Point out each Plasmodium parasite.
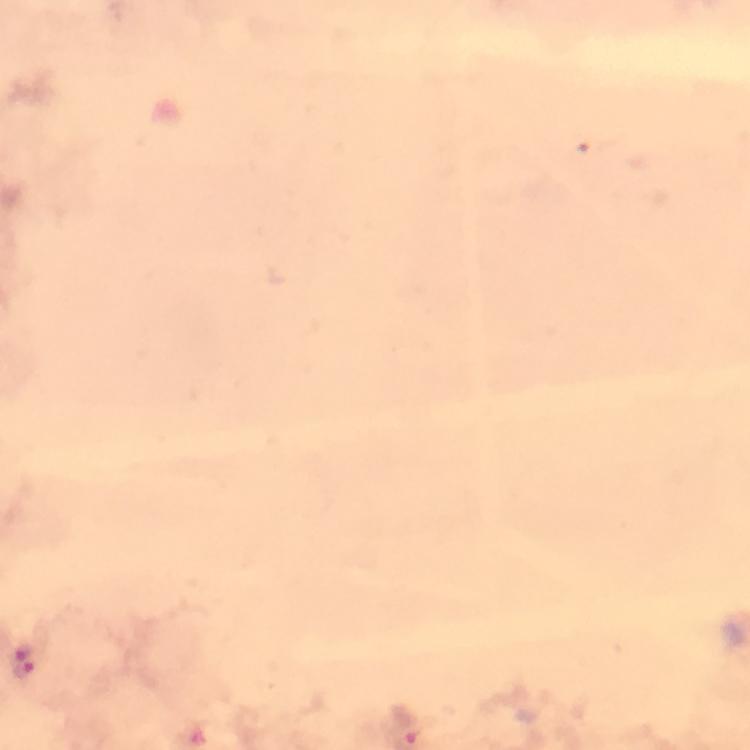

Approximate centers as {x, y} in pixels.
Plasmodium parasites: {21, 648}, {25, 672}.

Summary:
  - Stain: Giemsa
  - Immersion oil: used
  - Cropped from: a single field of view
  - Preparation: thick blood smear
  - Magnification: 100x
  - Image size: 750×750 pixels
  - Capture: smartphone mounted on the microscope
  - Context: from a diagnostic examination for malaria